State which parasite is depicted.
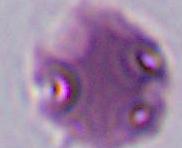
Plasmodium.

Summary:
  - Magnification: 400x or 1000x
  - Modality: micrograph